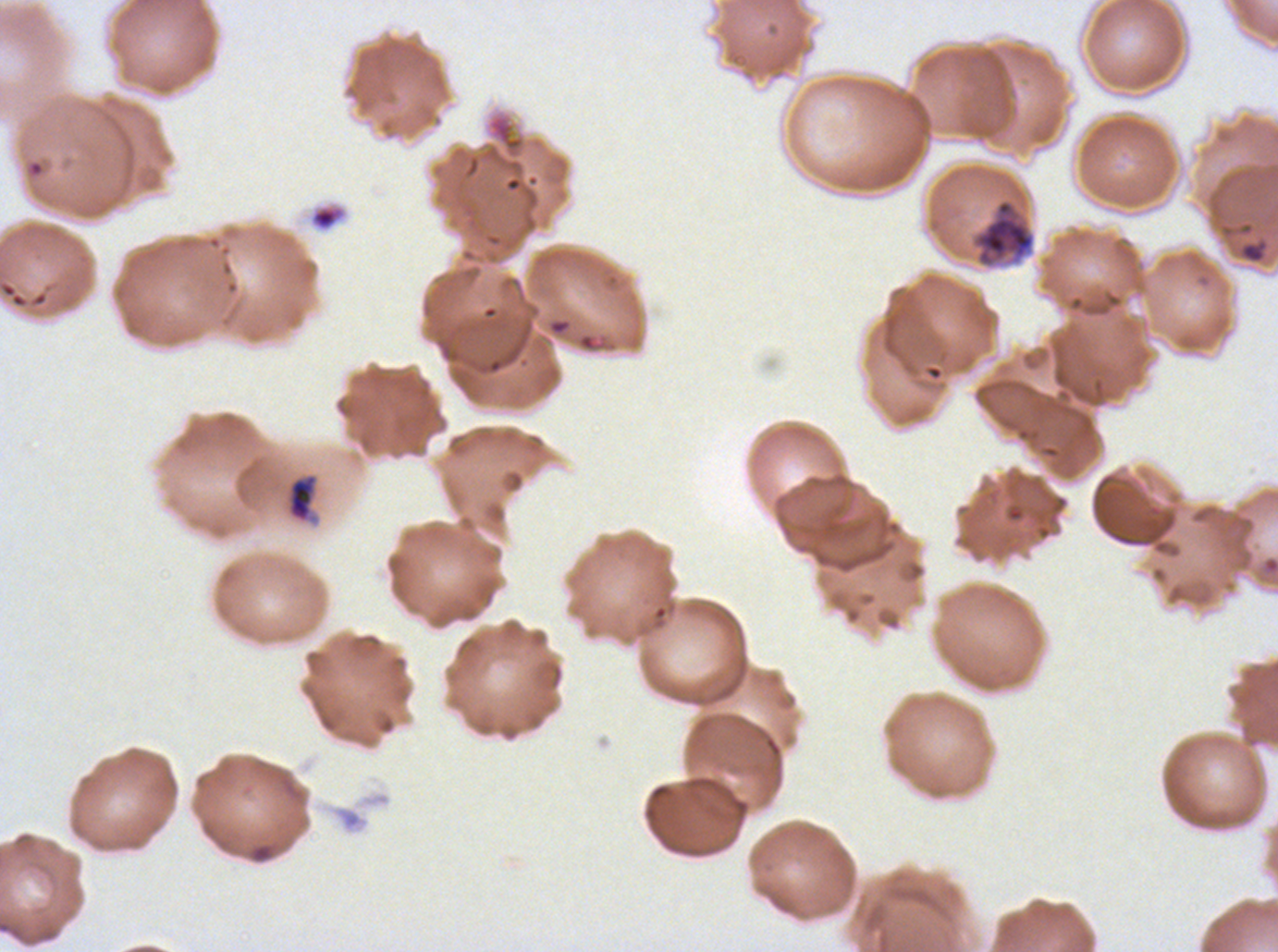

Approximate bounding boxes as (x1, y1, x2, y2) in pixels.
Summary:
  - Debris locations: (309, 203, 347, 232), (288, 475, 315, 521), (248, 842, 275, 863)
  - Mid trophozoite locations: (969, 197, 1037, 270)
  - Image size: 1278×952 pixels
  - Field of view: sub-image separated from a larger composite
  - Preparation: thin blood smear
  - Stain: Giemsa
  - Specimen: ex-vivo Plasmodium falciparum culture from a patient in The Gambia, grown for 24 to 48 hours